Report the malaria status of this cell.
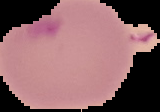
It is parasitized.

Image is 160×112 pixels. The area outside the segmented cell region is set to black. From a thin blood film.